Assess this cell for malaria.
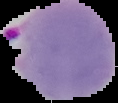
Parasitized.

From a thin blood film. Segmented cell region on a black background. Image is 118×103 pixels.